Report the malaria status of this cell.
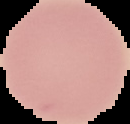

Uninfected.

Segmented cell region on a black background. Image is 130×124 pixels. From a thin blood film.